Report the malaria status of this cell.
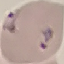
Parasitized.

Summary:
  - Stain: Giemsa
  - Capture: smartphone camera at the microscope eyepiece
  - Preparation: thin blood smear
  - Image type: cell patch, automatically extracted from a larger field of view and resized to 64 × 64 pixels